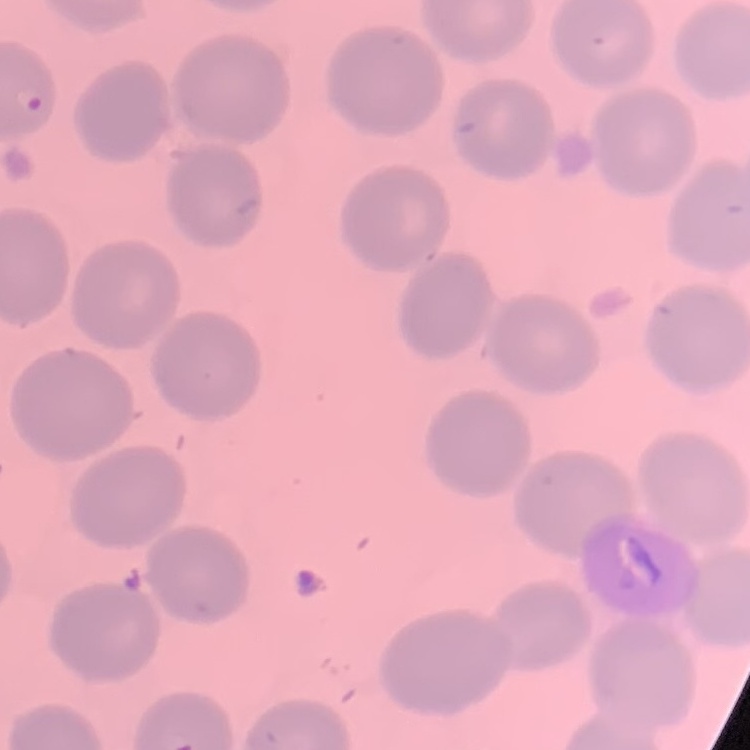
red blood cell morphology = no rouleaux formation
preparation = thin blood smear
stain = Field's or Giemsa
image type = one tile cut from a larger photomicrograph